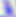

magnification = 400x
modality = photomicrograph
identification = Toxoplasma gondii